Locate every leukocyte (white blood cell).
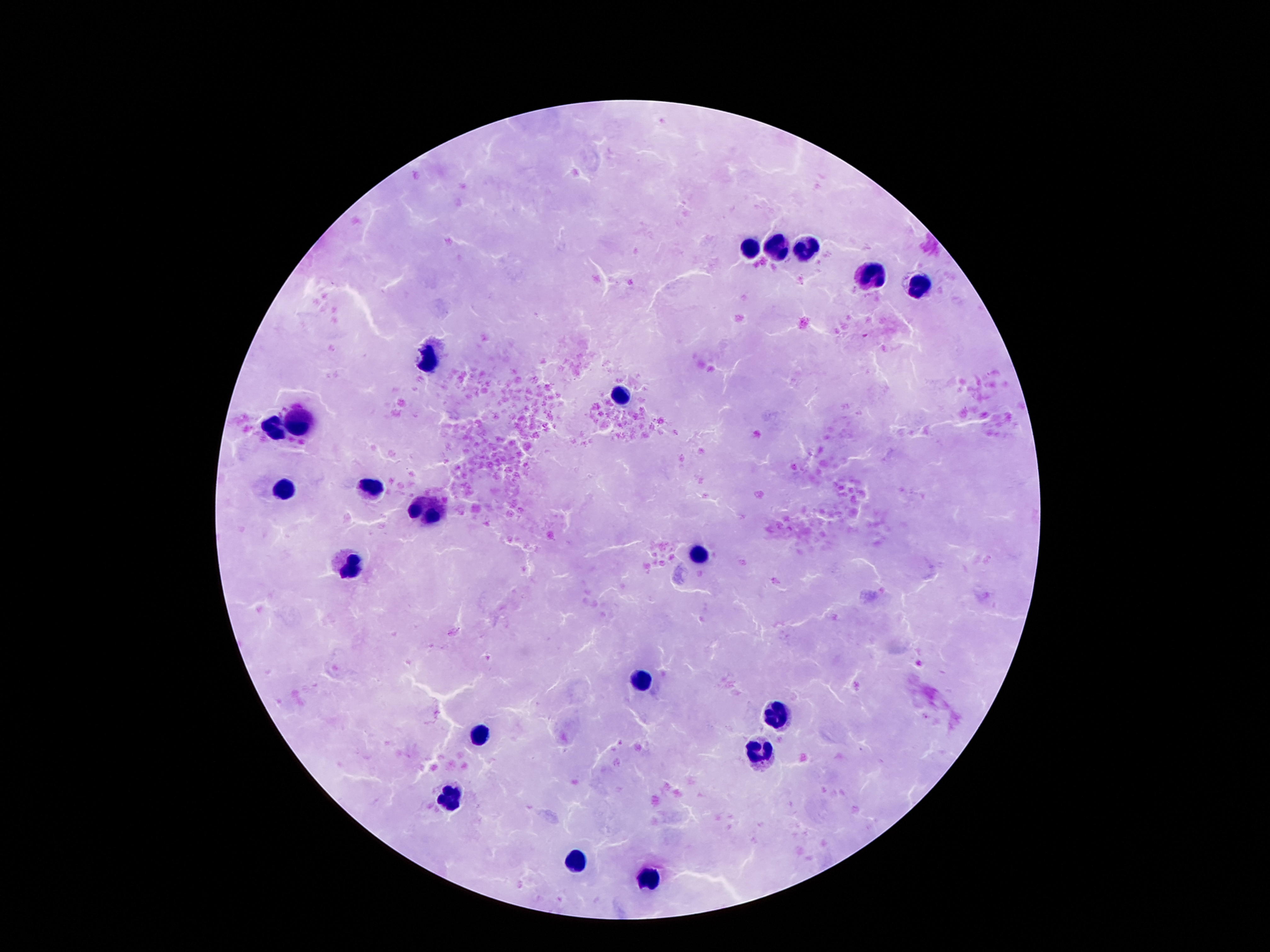

Approximate centers as [x, y] in pixels.
Leukocytes: [776, 244], [751, 245], [807, 248], [868, 273], [919, 282], [434, 360], [623, 397], [301, 420], [273, 428], [284, 486], [368, 486], [431, 505], [699, 556], [354, 565], [637, 678], [776, 716], [482, 731], [760, 756], [450, 798], [578, 861], [648, 878].

patient malaria status = not infected
field of view = single
capture = smartphone camera through the microscope eyepiece
preparation = thick blood smear
image size = 1270×952 pixels
magnification = 100x
stain = Giemsa